Assess the morphology of the erythrocytes.
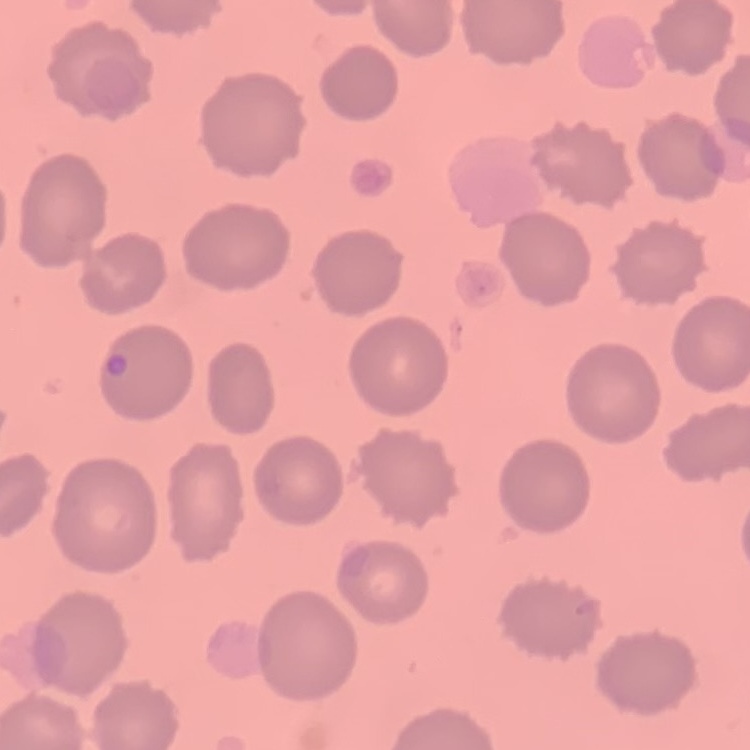

No rouleaux formation.

{
  "image_type": "square crop of a larger photomicrograph",
  "stain": "Field's or Giemsa",
  "preparation": "thin peripheral smear"
}